Give the extent of all uninfected red blood cells.
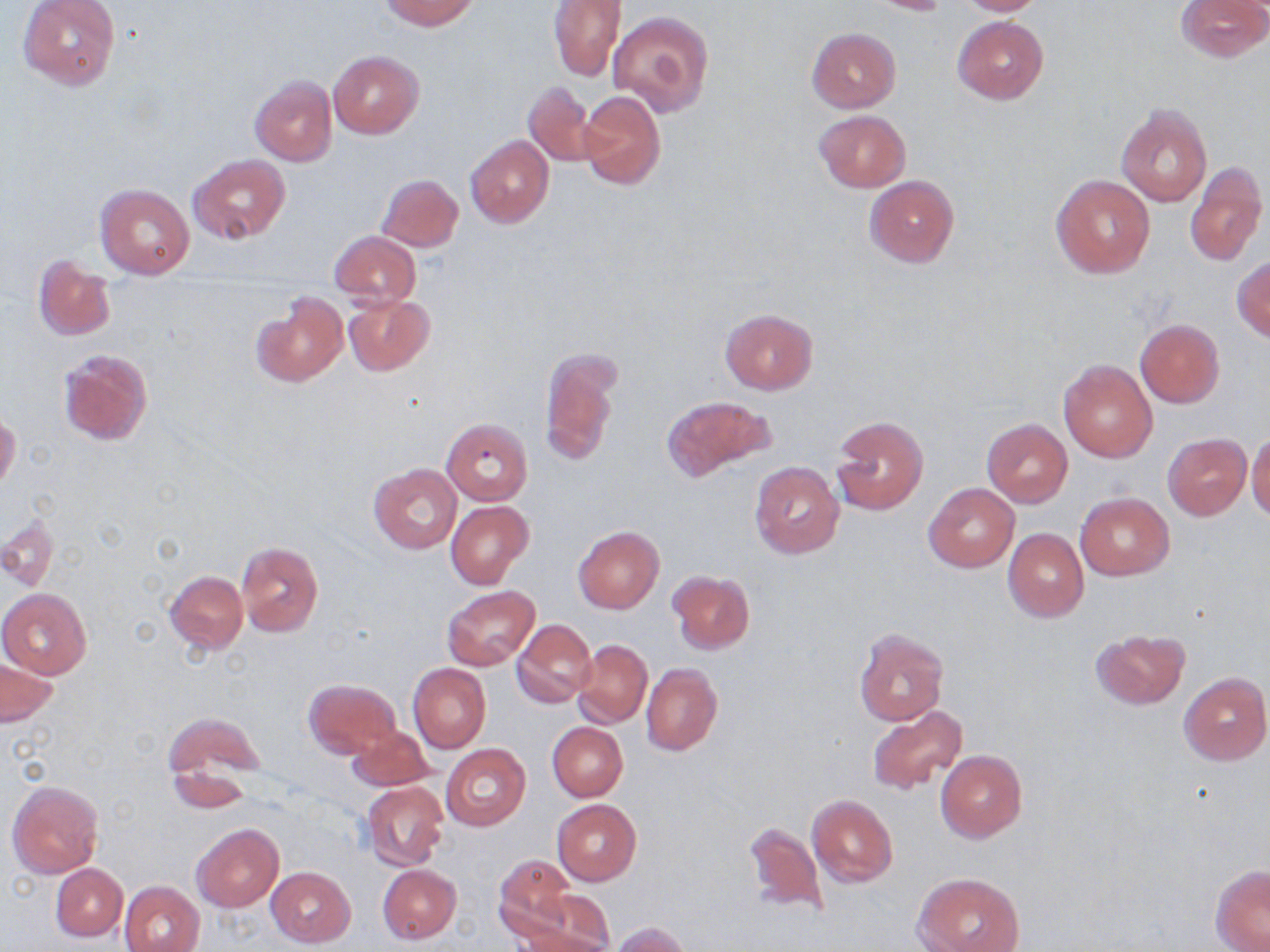
Approximate bounding boxes as (x1,y1)-(x2,y2) corner pairs in pixels.
Uninfected red blood cells: (18,0)-(121,89), (380,0)-(478,30), (548,0)-(626,82), (863,0)-(952,15), (954,0)-(1048,16), (1176,0)-(1269,62), (608,10)-(713,117), (953,16)-(1048,104), (806,28)-(901,113), (327,50)-(424,138), (250,66)-(420,155), (249,75)-(337,166), (523,82)-(598,167), (579,90)-(666,191), (1116,103)-(1212,207), (814,109)-(910,191), (465,135)-(554,229), (189,154)-(290,245), (1185,161)-(1266,269), (376,173)-(463,251), (863,175)-(959,268), (1053,175)-(1155,279), (95,184)-(195,279), (330,230)-(421,307), (32,254)-(116,340), (1232,255)-(1270,342), (250,291)-(346,386), (343,295)-(434,376), (720,309)-(818,395), (1134,318)-(1224,407), (538,347)-(620,468), (57,348)-(153,445), (1058,359)-(1157,463), (661,394)-(779,484), (0,414)-(21,493), (829,415)-(928,516), (442,418)-(533,504), (980,418)-(1073,507), (1247,427)-(1270,520), (1163,434)-(1252,519), (749,461)-(844,558), (369,464)-(462,554), (923,483)-(1019,572), (1075,493)-(1174,580), (446,500)-(535,589), (2,513)-(59,593), (573,527)-(664,613), (1002,528)-(1089,622), (236,542)-(324,638), (163,570)-(248,654), (668,572)-(754,654), (442,585)-(540,672), (0,589)-(91,678), (512,619)-(597,708), (1090,628)-(1190,710), (853,629)-(947,726), (572,638)-(653,728), (1,660)-(58,726), (408,663)-(490,753), (641,663)-(722,757), (1179,672)-(1269,765), (303,678)-(400,758), (864,704)-(969,797), (165,713)-(266,801), (547,722)-(627,800), (347,727)-(432,791), (441,743)-(531,831), (935,750)-(1028,842), (7,780)-(104,880), (362,781)-(448,873), (807,795)-(898,887), (552,799)-(642,885), (741,820)-(828,918), (192,823)-(284,912), (493,854)-(576,941), (51,863)-(128,940), (378,864)-(461,944), (1211,865)-(1270,951), (266,867)-(356,948), (917,872)-(1024,952), (121,879)-(205,952), (525,887)-(616,950), (612,922)-(691,952), (513,924)-(614,952).

{
  "slide_level_diagnosis": "negative for blood parasites",
  "modality": "optical microscopy",
  "stain": "May-Grünwald-Giemsa",
  "image_size": "1270×952 pixels",
  "field_of_view": "one of a larger specimen",
  "preparation": "thin blood film",
  "magnification": "1000x"
}